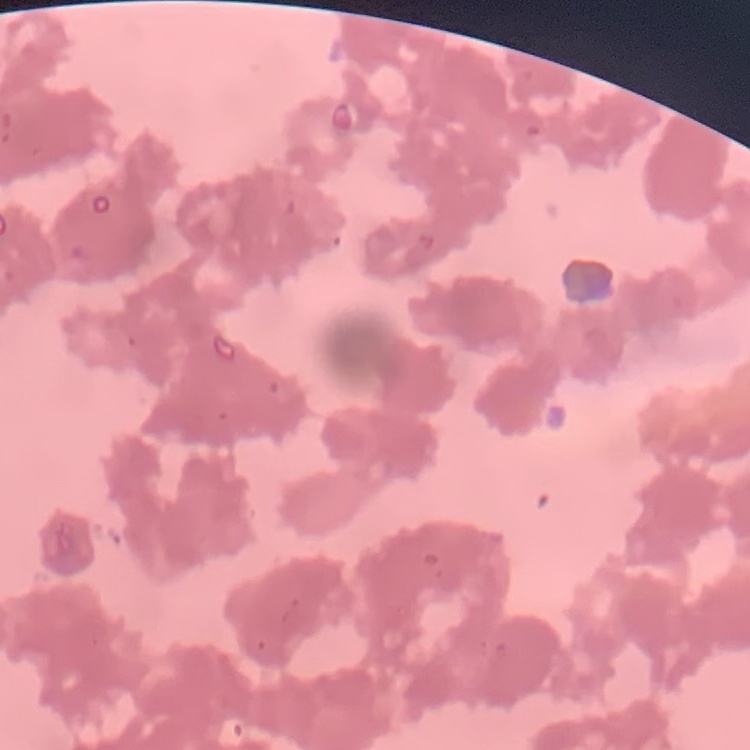 The red blood cells exhibit rouleaux formation. Thin blood smear. Stained with either Field's or Giemsa. Square crop of a larger photomicrograph.